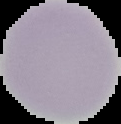

image_size: 121×124 pixels
malaria_status: uninfected
image_type: segmented cell region on a black background
preparation: thin blood smear